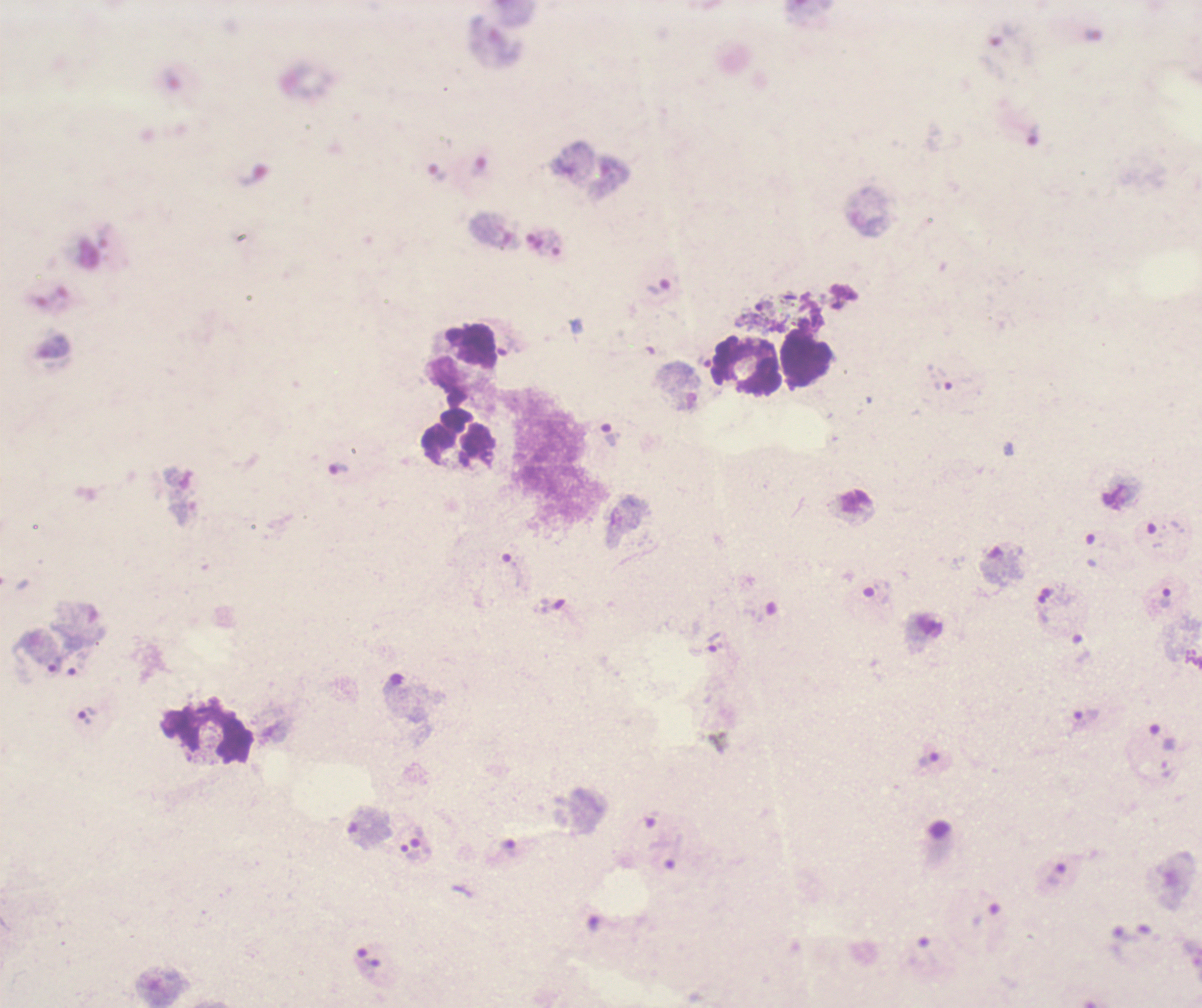
stain: Romanowsky
result: Plasmodium parasites detected
leukocyte_locations: 'approximate object centers, in pixels from the top-left corner: (x=748, y=366), (x=459, y=437), (x=209, y=735)'
trophozoite_locations: 'approximate object centers, in pixels from the top-left corner: (x=660, y=287), (x=611, y=436), (x=1166, y=598), (x=715, y=641), (x=88, y=716), (x=1163, y=737)'
background_quality: unsatisfactory
magnification: 100x
image_size: 1202×1008 pixels
preparation: thick blood film
context: previously used in a real diagnosis
field_of_view: single
coloration_quality: bad